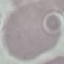
result = no malaria parasites seen
stain = Giemsa
capture = smartphone through the microscope eyepiece
image type = automatically extracted cell patch, resized to 64 × 64 pixels
preparation = thin blood smear